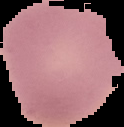

Summary:
  - Image type: segmented cell region on a black background
  - Preparation: thin blood film
  - Image size: 124×127 pixels
  - Result: no malaria parasites detected